Locate every blood parasite and identify its species.
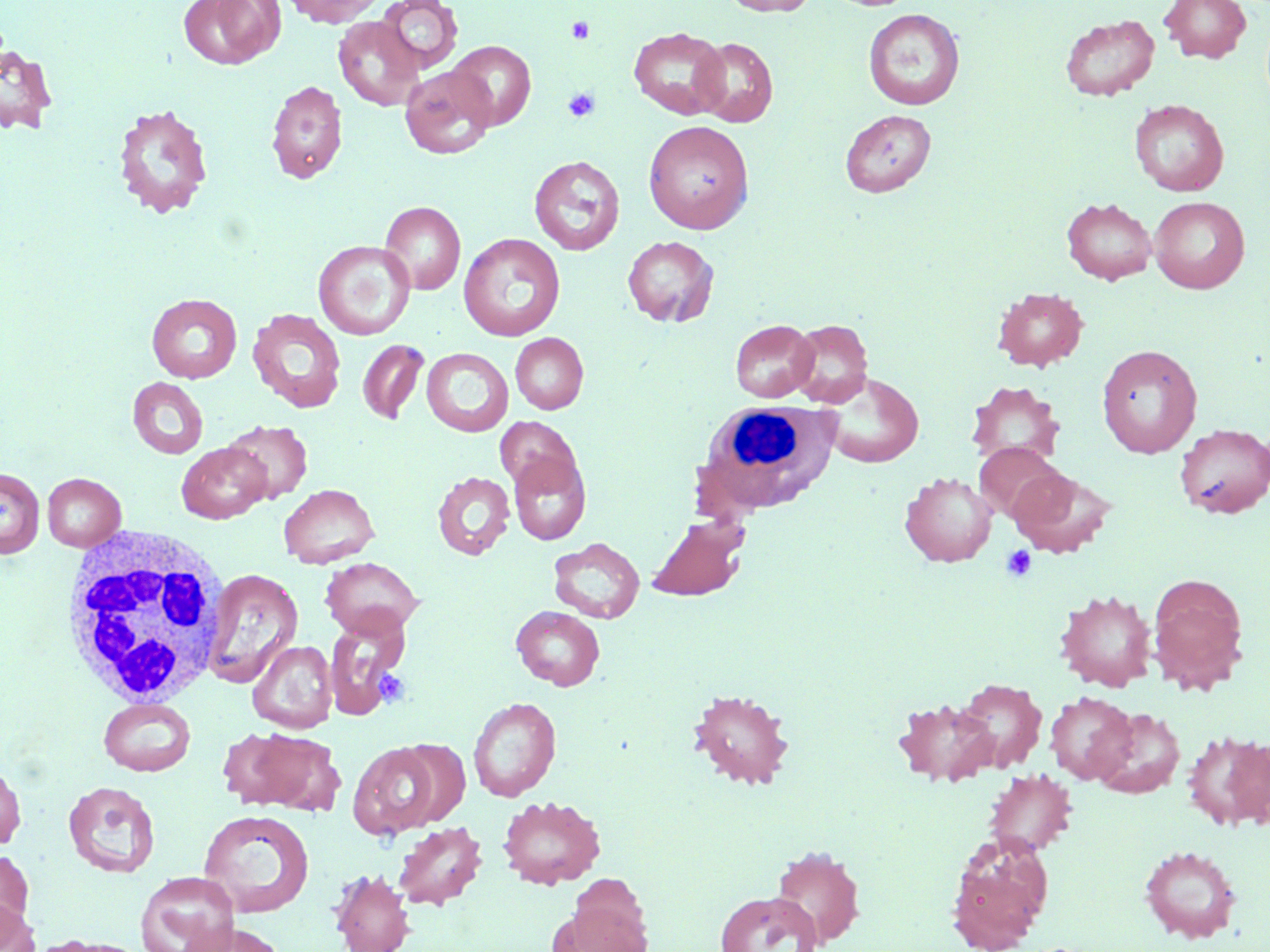
No blood parasites seen.

Summary:
  - Coordinate format: approximate bounding boxes as (x1, y1, x2, y2) in pixels
  - Platelet locations: (567, 17, 594, 43), (563, 87, 601, 123), (1001, 545, 1036, 582), (374, 668, 410, 708)
  - Uninfected red blood cell locations: (178, 0, 284, 69), (280, 0, 387, 27), (376, 0, 463, 74), (721, 0, 819, 16), (1159, 0, 1252, 63), (863, 8, 965, 110), (1060, 13, 1160, 101), (332, 15, 425, 111), (628, 27, 730, 120), (692, 37, 778, 127), (448, 40, 536, 131), (0, 44, 57, 134), (399, 65, 498, 159), (266, 79, 348, 184), (1129, 99, 1229, 196), (112, 102, 214, 219), (840, 109, 936, 197), (643, 120, 754, 233), (529, 155, 625, 255), (1149, 196, 1250, 293), (1062, 197, 1157, 285), (379, 201, 465, 294), (458, 233, 566, 341), (622, 235, 719, 327), (313, 240, 415, 340), (992, 287, 1089, 371), (147, 293, 242, 383), (247, 307, 347, 414), (730, 319, 818, 402), (787, 319, 873, 407), (510, 333, 588, 414), (357, 340, 429, 424), (1096, 344, 1203, 458), (421, 347, 513, 437), (816, 371, 924, 468), (128, 377, 208, 459), (966, 381, 1065, 466), (495, 416, 580, 493), (223, 420, 313, 504), (1176, 422, 1270, 519), (177, 442, 271, 523), (974, 442, 1065, 522), (508, 452, 591, 545), (1007, 466, 1116, 558), (0, 467, 44, 558), (432, 471, 515, 560), (900, 472, 997, 567), (42, 473, 126, 551), (279, 483, 379, 568), (647, 516, 748, 601), (548, 537, 645, 623), (321, 557, 423, 639), (202, 568, 304, 686), (1148, 573, 1250, 693), (1055, 589, 1158, 691), (511, 606, 605, 690), (324, 613, 410, 719), (247, 640, 337, 733), (954, 678, 1046, 772), (688, 687, 795, 790), (1045, 691, 1137, 785), (468, 697, 560, 802), (98, 698, 196, 776), (893, 698, 998, 788), (1093, 707, 1185, 799), (216, 727, 304, 809), (247, 729, 346, 816), (1183, 730, 1270, 831), (349, 742, 441, 839), (0, 760, 27, 850), (983, 769, 1078, 857), (63, 781, 160, 878), (497, 795, 606, 889), (198, 809, 315, 918), (392, 821, 487, 910), (946, 832, 1053, 951), (769, 845, 866, 949), (1139, 845, 1242, 943), (0, 848, 34, 938), (329, 869, 415, 952), (135, 871, 239, 952), (563, 877, 653, 952), (715, 891, 822, 952), (0, 899, 40, 952), (180, 921, 286, 951), (33, 936, 147, 952)
  - White blood cell locations: (696, 400, 838, 514), (60, 523, 231, 710)
  - Slide-level diagnosis: no evidence of blood parasites
  - Image size: 1270×952 pixels
  - Magnification: 1000x
  - Stain: May-Grünwald-Giemsa
  - Modality: light microscopy
  - Field of view: single
  - Preparation: thin blood smear